Report the malaria status of this cell.
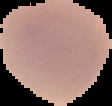

It is uninfected.

image_type: cell region segmented out of the field of view; surrounding area masked to black
preparation: thin blood smear
image_size: 112×106 pixels